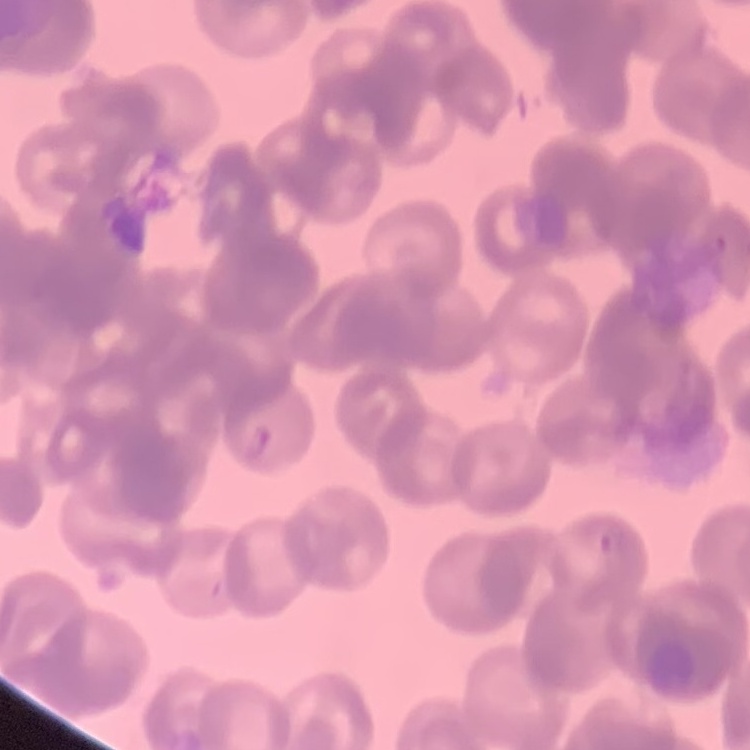

The erythrocytes exhibit rouleaux formation. Stained with either Field's or Giemsa. Square crop of a larger photomicrograph. Thin peripheral smear.